Locate and identify every blood parasite.
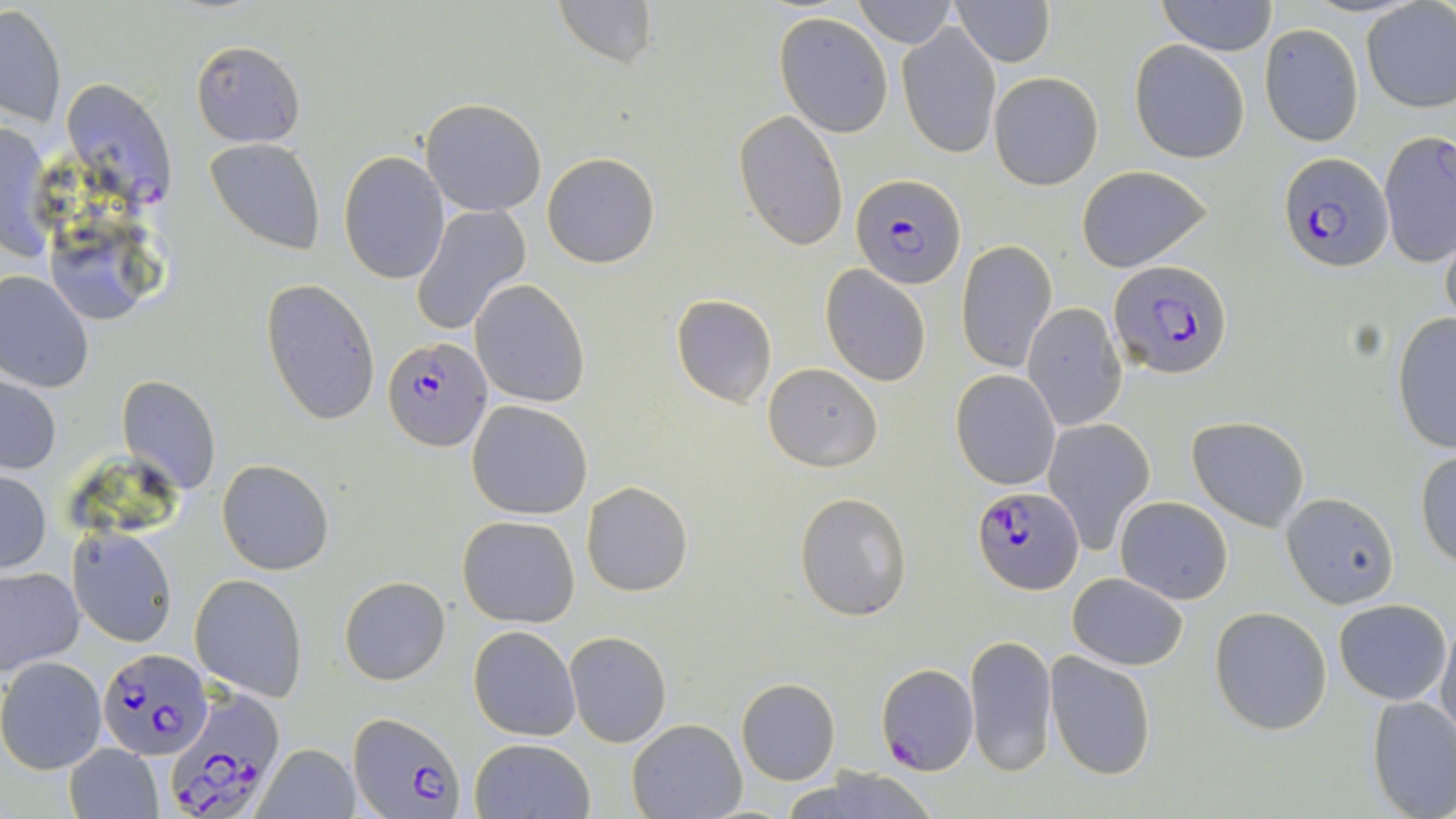

Approximate bounding boxes as [x1, y1, x2, y2] in pixels.
Plasmodium falciparum-infected red blood cells: [60, 78, 176, 205], [1279, 152, 1392, 271], [852, 174, 966, 290], [1111, 262, 1233, 379], [382, 336, 493, 454], [972, 487, 1082, 593], [98, 648, 213, 759], [877, 662, 978, 773], [161, 686, 285, 816], [348, 709, 463, 819].
No Plasmodium ovale, Plasmodium malariae, Plasmodium vivax, Babesia divergens, or Trypanosoma brucei observed.

Summary:
  - Uninfected red blood cell locations: [553, 0, 659, 71], [853, 0, 955, 46], [952, 0, 1054, 68], [1157, 0, 1277, 55], [1360, 2, 1456, 114], [1, 4, 68, 128], [773, 12, 893, 137], [898, 21, 1002, 159], [1258, 23, 1364, 144], [190, 39, 304, 146], [1131, 41, 1249, 164], [989, 72, 1103, 190], [420, 98, 546, 217], [734, 111, 849, 251], [0, 120, 53, 263], [1378, 132, 1456, 268], [204, 137, 326, 255], [338, 152, 449, 284], [542, 153, 659, 268], [1076, 165, 1212, 273], [410, 204, 531, 336], [1439, 224, 1456, 336], [955, 241, 1057, 374], [822, 266, 931, 386], [0, 270, 95, 393], [261, 279, 381, 426], [470, 279, 590, 408], [670, 293, 777, 408], [1023, 303, 1126, 430], [1391, 314, 1456, 452], [762, 363, 883, 471], [950, 369, 1061, 490], [1, 372, 62, 477], [116, 374, 221, 496], [466, 400, 593, 519], [1188, 416, 1310, 530], [1044, 418, 1154, 553], [1416, 449, 1456, 568], [217, 460, 334, 575], [0, 470, 50, 574], [582, 481, 693, 597], [795, 491, 912, 620], [1281, 491, 1400, 607], [1115, 496, 1233, 604], [458, 516, 580, 626], [67, 526, 178, 648], [0, 565, 84, 674], [1066, 573, 1188, 670], [190, 574, 309, 701], [340, 577, 450, 684], [1333, 598, 1451, 705], [1209, 606, 1332, 735], [1437, 618, 1456, 745], [468, 626, 580, 741], [565, 631, 672, 748], [965, 635, 1058, 775], [1045, 653, 1156, 778], [0, 656, 106, 773], [736, 679, 839, 785], [1366, 697, 1456, 819], [626, 719, 746, 819], [470, 737, 595, 819], [63, 743, 165, 819], [257, 743, 359, 819], [782, 767, 946, 819]
  - Slide-level diagnosis: Plasmodium falciparum
  - Field of view: single
  - Magnification: 1000x
  - Modality: optical microscopy
  - Preparation: thin blood smear
  - Stain: May-Grünwald-Giemsa
  - Image size: 1456×819 pixels